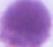

Summary:
  - Identification: erythrocyte
  - Magnification: 1000x
  - Modality: photomicrograph